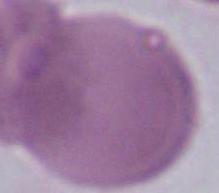
magnification = 1000x
identification = red blood cell
modality = micrograph